Classify this cell by malaria status.
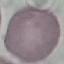
Uninfected.

image type = automatically extracted cell patch, resized to 64 × 64 pixels
stain = Giemsa
capture = smartphone through the microscope eyepiece
preparation = thin smear